Describe the morphology of the red blood cells.
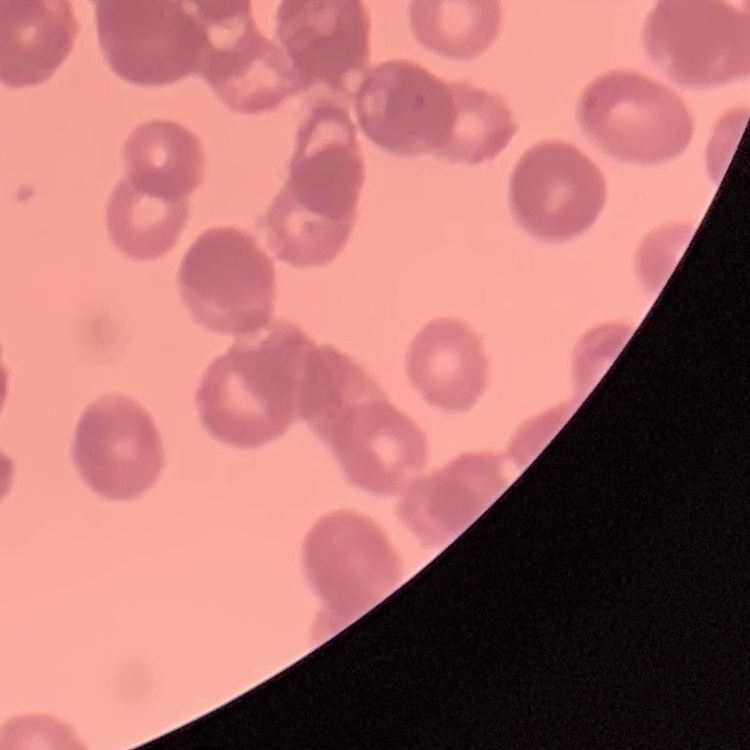

Rouleaux formation.

{
  "preparation": "thin peripheral smear",
  "image_type": "square crop of a larger photomicrograph",
  "stain": "Field's or Giemsa"
}